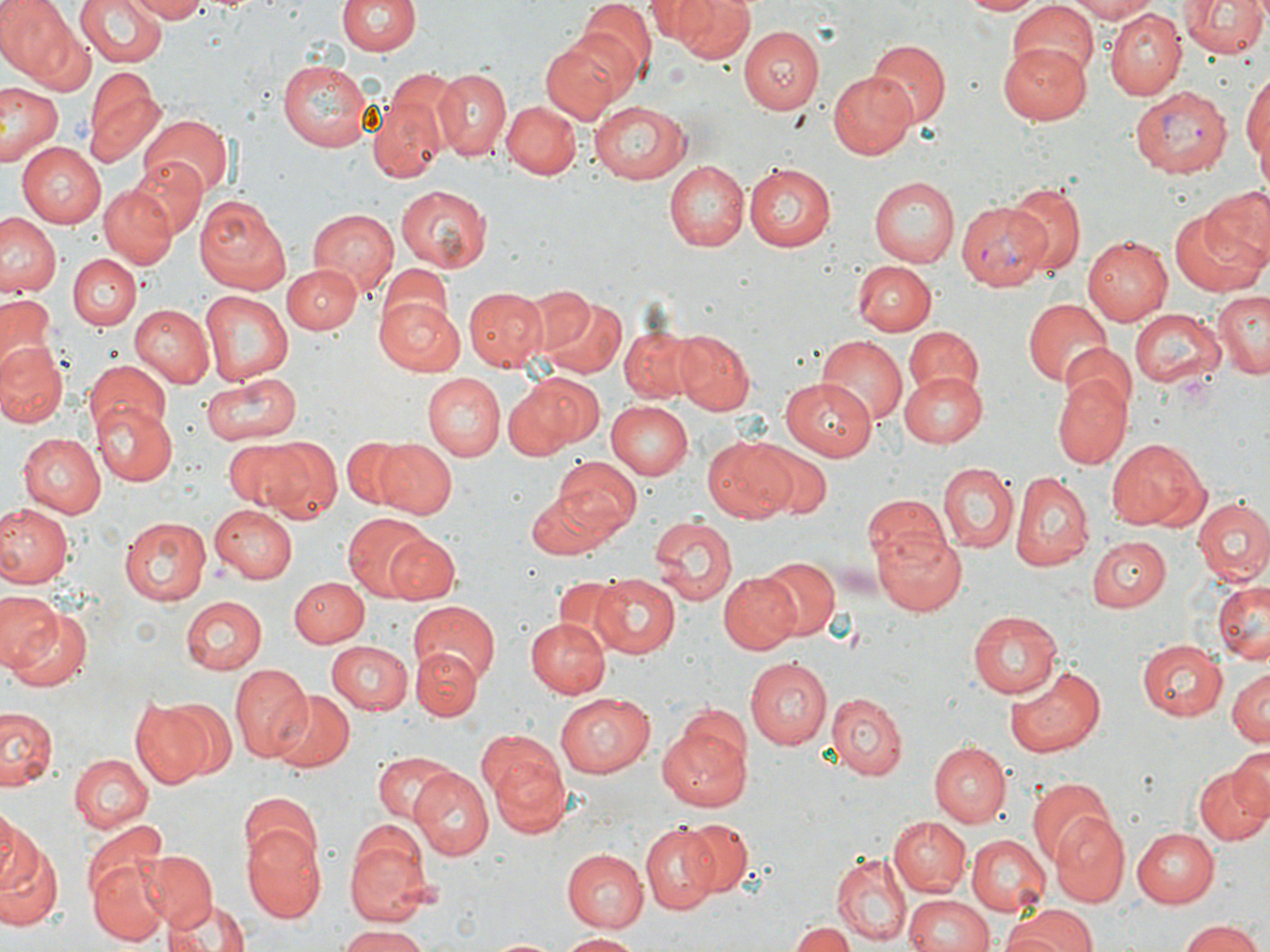

{
  "slide_level_diagnosis": "Plasmodium vivax",
  "stain": "May-Grünwald-Giemsa",
  "preparation": "thin blood film",
  "modality": "light microscopy",
  "magnification": "1000x",
  "field_of_view": "one of a larger specimen",
  "uninfected_red_blood_cell_locations": "approximate bounding boxes as named x1/y1/x2/y2 corners in pixels: (x1=0, y1=0, x2=69, y2=74), (x1=73, y1=0, x2=167, y2=69), (x1=128, y1=0, x2=209, y2=23), (x1=646, y1=0, x2=712, y2=42), (x1=662, y1=0, x2=758, y2=62), (x1=959, y1=0, x2=1046, y2=16), (x1=1061, y1=0, x2=1157, y2=22), (x1=1175, y1=0, x2=1269, y2=62), (x1=339, y1=1, x2=419, y2=58), (x1=574, y1=1, x2=654, y2=83), (x1=1007, y1=3, x2=1102, y2=82), (x1=1106, y1=9, x2=1185, y2=99), (x1=20, y1=15, x2=96, y2=93), (x1=740, y1=27, x2=825, y2=114), (x1=540, y1=35, x2=628, y2=122), (x1=868, y1=38, x2=950, y2=130), (x1=996, y1=46, x2=1091, y2=126), (x1=277, y1=57, x2=373, y2=152), (x1=1242, y1=68, x2=1269, y2=182), (x1=83, y1=69, x2=163, y2=169), (x1=433, y1=69, x2=512, y2=160), (x1=829, y1=70, x2=921, y2=159), (x1=0, y1=83, x2=64, y2=168), (x1=369, y1=91, x2=446, y2=185), (x1=501, y1=100, x2=580, y2=179), (x1=589, y1=100, x2=692, y2=183), (x1=137, y1=115, x2=232, y2=199), (x1=17, y1=142, x2=109, y2=227), (x1=127, y1=155, x2=206, y2=241), (x1=663, y1=160, x2=749, y2=250), (x1=744, y1=163, x2=837, y2=252), (x1=868, y1=175, x2=959, y2=267), (x1=1003, y1=182, x2=1087, y2=275), (x1=97, y1=183, x2=175, y2=269), (x1=395, y1=184, x2=492, y2=275), (x1=1202, y1=186, x2=1270, y2=272), (x1=195, y1=194, x2=293, y2=293), (x1=305, y1=207, x2=399, y2=293), (x1=1169, y1=207, x2=1266, y2=296), (x1=1, y1=213, x2=62, y2=298), (x1=1081, y1=235, x2=1171, y2=326), (x1=68, y1=254, x2=140, y2=330), (x1=851, y1=260, x2=936, y2=335), (x1=283, y1=263, x2=362, y2=333), (x1=383, y1=263, x2=452, y2=327), (x1=517, y1=285, x2=595, y2=361), (x1=464, y1=287, x2=547, y2=371), (x1=197, y1=290, x2=295, y2=385), (x1=1210, y1=291, x2=1270, y2=377), (x1=0, y1=293, x2=59, y2=368), (x1=375, y1=294, x2=465, y2=375), (x1=538, y1=297, x2=625, y2=378), (x1=1023, y1=297, x2=1111, y2=386), (x1=129, y1=305, x2=214, y2=388), (x1=1128, y1=305, x2=1226, y2=389), (x1=621, y1=326, x2=704, y2=404), (x1=902, y1=326, x2=985, y2=405), (x1=674, y1=330, x2=755, y2=415), (x1=818, y1=336, x2=906, y2=422), (x1=1065, y1=342, x2=1136, y2=413), (x1=0, y1=343, x2=68, y2=427), (x1=84, y1=360, x2=171, y2=439), (x1=199, y1=370, x2=300, y2=445), (x1=900, y1=370, x2=987, y2=447), (x1=509, y1=372, x2=603, y2=455), (x1=1054, y1=372, x2=1131, y2=471), (x1=423, y1=374, x2=504, y2=459), (x1=782, y1=379, x2=873, y2=460), (x1=605, y1=401, x2=693, y2=480), (x1=94, y1=405, x2=177, y2=486), (x1=17, y1=433, x2=103, y2=516), (x1=341, y1=436, x2=411, y2=510), (x1=702, y1=437, x2=797, y2=523), (x1=1108, y1=438, x2=1209, y2=531), (x1=253, y1=439, x2=340, y2=521), (x1=221, y1=440, x2=309, y2=512), (x1=377, y1=440, x2=457, y2=518), (x1=750, y1=442, x2=830, y2=517), (x1=551, y1=458, x2=642, y2=541), (x1=935, y1=461, x2=1018, y2=551), (x1=1011, y1=472, x2=1092, y2=569), (x1=526, y1=493, x2=615, y2=562), (x1=864, y1=495, x2=952, y2=574), (x1=1192, y1=499, x2=1270, y2=587), (x1=210, y1=502, x2=298, y2=583), (x1=0, y1=504, x2=71, y2=589), (x1=343, y1=513, x2=436, y2=601), (x1=647, y1=515, x2=736, y2=606), (x1=120, y1=516, x2=209, y2=605), (x1=871, y1=527, x2=967, y2=615), (x1=384, y1=534, x2=460, y2=604), (x1=1088, y1=538, x2=1171, y2=612), (x1=756, y1=555, x2=840, y2=640), (x1=718, y1=571, x2=805, y2=653), (x1=591, y1=573, x2=681, y2=656), (x1=555, y1=576, x2=629, y2=649), (x1=291, y1=577, x2=366, y2=647), (x1=1213, y1=578, x2=1270, y2=663), (x1=0, y1=591, x2=60, y2=673), (x1=178, y1=596, x2=265, y2=676), (x1=406, y1=604, x2=500, y2=685), (x1=6, y1=608, x2=94, y2=695), (x1=966, y1=611, x2=1061, y2=698), (x1=524, y1=616, x2=610, y2=696), (x1=1136, y1=639, x2=1228, y2=722), (x1=326, y1=641, x2=414, y2=714), (x1=412, y1=649, x2=481, y2=720), (x1=744, y1=656, x2=833, y2=750), (x1=229, y1=663, x2=311, y2=763), (x1=1006, y1=667, x2=1106, y2=758), (x1=1227, y1=669, x2=1270, y2=748), (x1=267, y1=689, x2=353, y2=772), (x1=556, y1=691, x2=654, y2=779), (x1=825, y1=691, x2=908, y2=779), (x1=164, y1=697, x2=238, y2=780), (x1=129, y1=699, x2=212, y2=787), (x1=1, y1=706, x2=60, y2=793), (x1=658, y1=724, x2=752, y2=808), (x1=932, y1=743, x2=1010, y2=826), (x1=1225, y1=744, x2=1269, y2=827), (x1=483, y1=747, x2=573, y2=833), (x1=374, y1=751, x2=454, y2=824), (x1=70, y1=754, x2=153, y2=833), (x1=1193, y1=761, x2=1270, y2=845), (x1=407, y1=771, x2=494, y2=860), (x1=1027, y1=778, x2=1115, y2=867), (x1=238, y1=794, x2=320, y2=874), (x1=0, y1=813, x2=38, y2=895), (x1=1052, y1=814, x2=1129, y2=906), (x1=887, y1=815, x2=970, y2=896), (x1=682, y1=817, x2=754, y2=895), (x1=640, y1=822, x2=720, y2=912), (x1=241, y1=823, x2=325, y2=921), (x1=345, y1=825, x2=434, y2=926), (x1=1130, y1=826, x2=1218, y2=907), (x1=966, y1=834, x2=1049, y2=915), (x1=0, y1=845, x2=64, y2=931), (x1=87, y1=845, x2=169, y2=947), (x1=142, y1=849, x2=217, y2=930), (x1=561, y1=849, x2=647, y2=932), (x1=831, y1=852, x2=910, y2=945), (x1=154, y1=876, x2=233, y2=947), (x1=904, y1=894, x2=995, y2=952), (x1=168, y1=900, x2=249, y2=952), (x1=998, y1=904, x2=1100, y2=952), (x1=1179, y1=919, x2=1264, y2=952), (x1=788, y1=920, x2=854, y2=952), (x1=340, y1=926, x2=433, y2=952), (x1=554, y1=932, x2=644, y2=950)",
  "plasmodium_vivax_infected_red_blood_cell_locations": "approximate bounding boxes as named x1/y1/x2/y2 corners in pixels: (x1=1131, y1=85, x2=1236, y2=176), (x1=957, y1=201, x2=1052, y2=289)",
  "image_size": "1270×952 pixels"
}